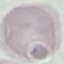
Result: no malaria parasites seen. Photographed with a smartphone camera at the microscope eyepiece. Automatically extracted cell patch, resized to 64 × 64 pixels. Giemsa-stained preparation. Thin blood film.